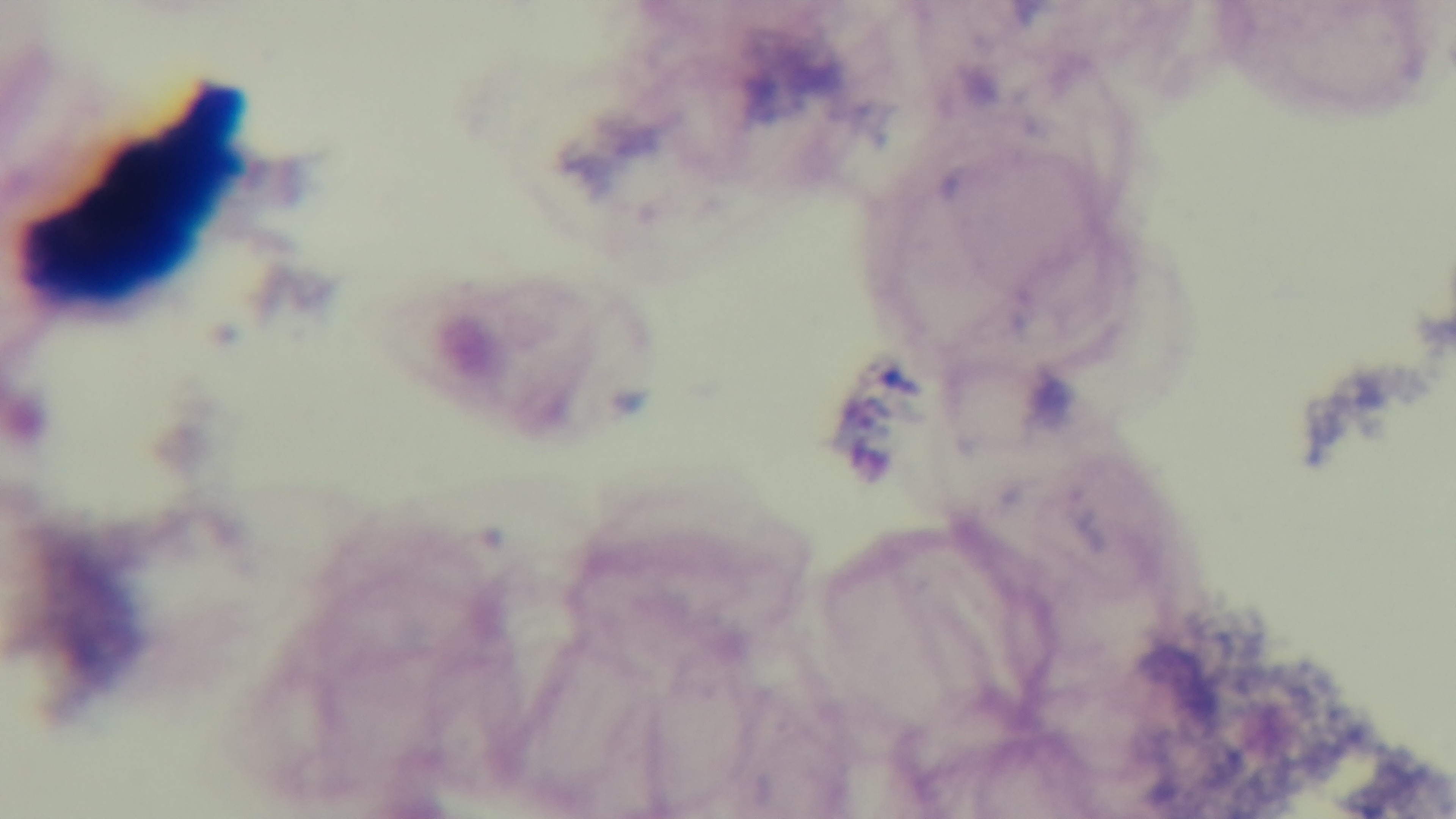
capture = mounted 4K digital camera
stain = Giemsa
preparation = thick blood film
field of view = single
objective = 100x oil immersion
modality = light microscopy
malaria status = uninfected